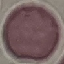

result: no malaria parasites detected
image_type: automatically extracted cell patch, resized to 64 × 64 pixels
stain: Giemsa
capture: smartphone camera at the microscope eyepiece
preparation: thin blood film